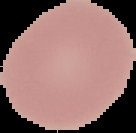

Summary:
  - Image size: 136×133 pixels
  - Malaria status: uninfected
  - Image type: segmented cell region on a black background
  - Preparation: thin blood smear